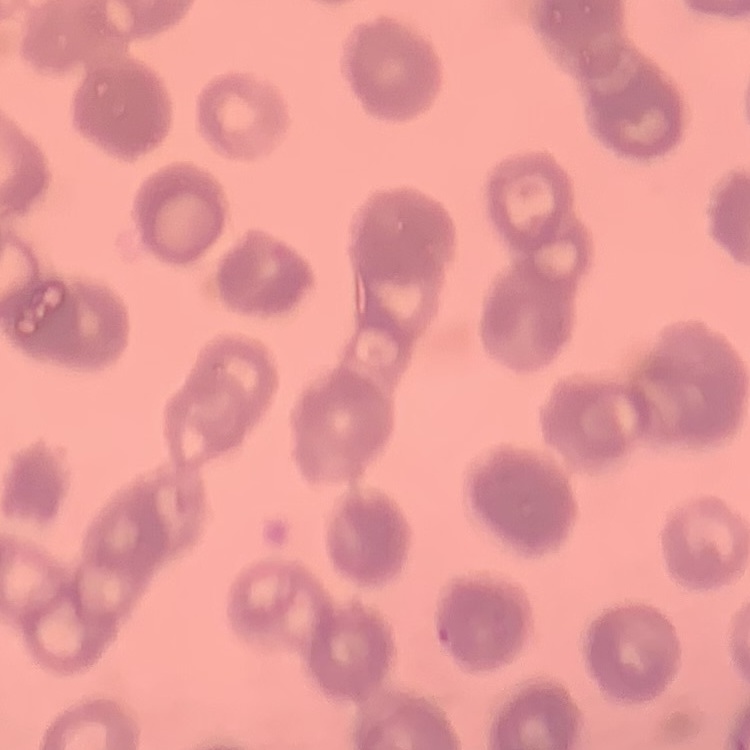
{
  "red_blood_cell_morphology": "rouleaux formation",
  "image_type": "square crop of a larger photomicrograph",
  "preparation": "thin blood film",
  "stain": "Field's or Giemsa"
}